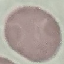

Result: no malaria parasites detected. Giemsa-stained preparation. Thin smear of blood. Photographed with a smartphone camera at the microscope eyepiece. Automatically extracted cell patch, resized to 64 × 64 pixels.